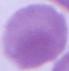

Summary:
  - Identification: red blood cell
  - Magnification: 1000x
  - Modality: photomicrograph